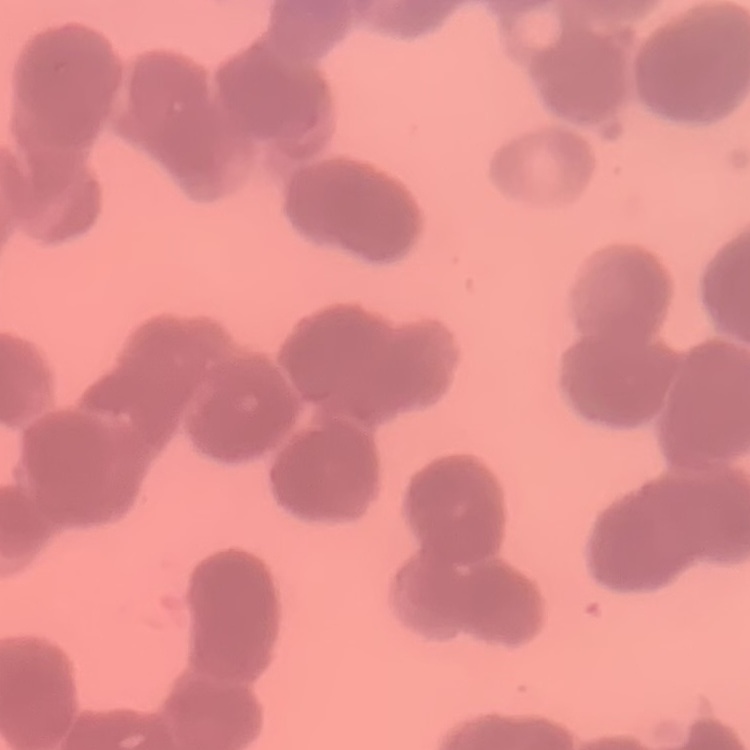

red blood cell morphology = rouleaux formation
preparation = thin peripheral smear
image type = square crop of a larger photomicrograph
stain = Field's or Giemsa